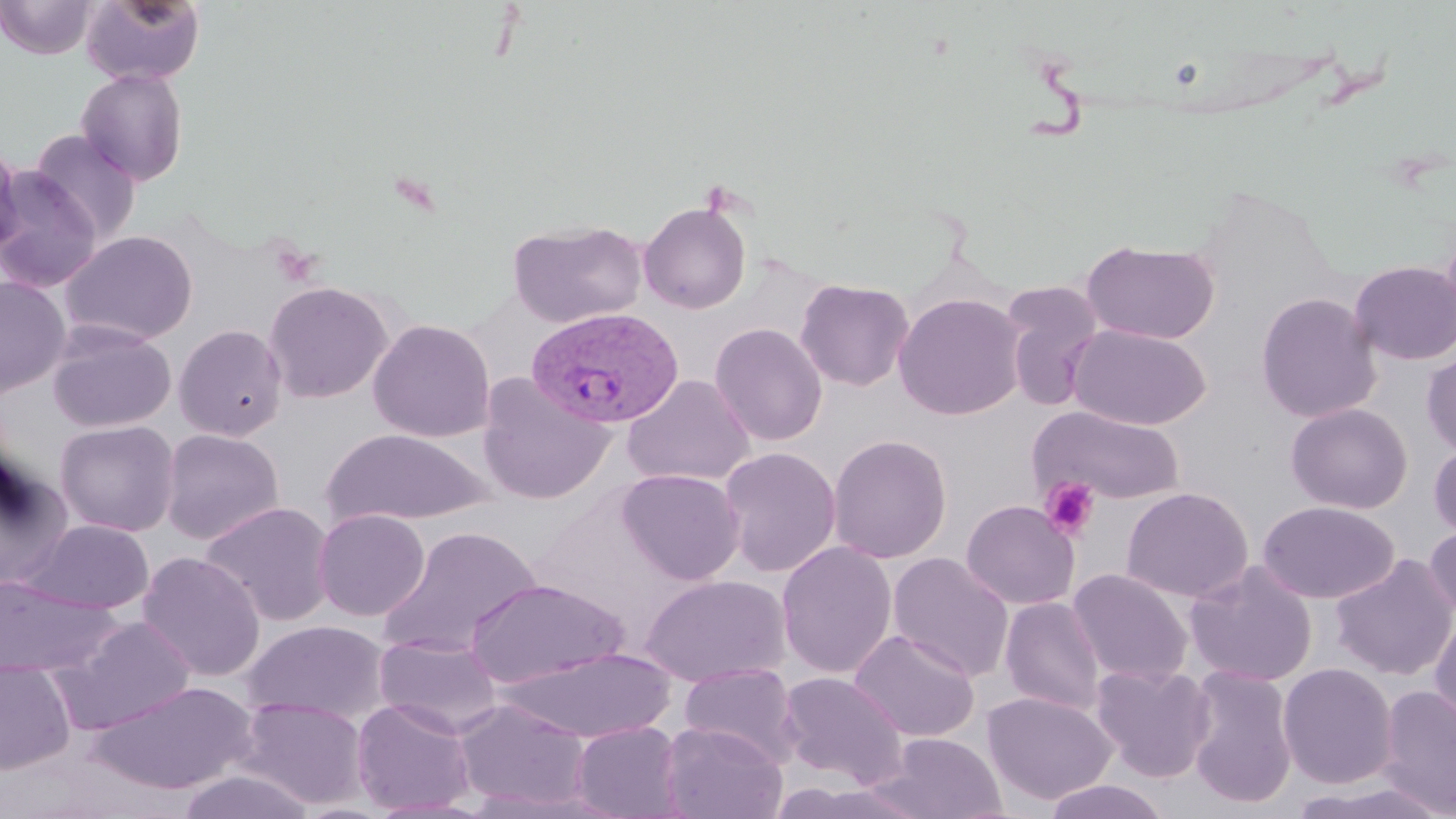
Summary:
  - Coordinate format: approximate bounding boxes as (x1, y1, x2, y2) in pixels
  - Plasmodium vivax-infected red blood cell locations: (527, 307, 683, 430)
  - Uninfected red blood cell locations: (1, 0, 95, 59), (81, 0, 206, 85), (76, 68, 189, 186), (30, 129, 142, 243), (0, 146, 24, 256), (0, 167, 103, 290), (638, 198, 752, 314), (507, 220, 647, 328), (61, 231, 198, 345), (1081, 238, 1219, 345), (1349, 260, 1456, 365), (0, 276, 70, 399), (795, 278, 914, 391), (263, 280, 393, 404), (1001, 281, 1105, 411), (893, 292, 1027, 420), (1256, 292, 1382, 422), (368, 318, 496, 443), (48, 323, 176, 433), (710, 323, 828, 446), (173, 324, 288, 441), (1067, 324, 1212, 430), (1421, 348, 1456, 457), (477, 375, 615, 505), (622, 375, 756, 487), (1285, 402, 1412, 514), (1029, 405, 1187, 505), (54, 420, 180, 537), (160, 429, 283, 544), (320, 429, 496, 527), (828, 434, 952, 564), (1428, 440, 1456, 544), (719, 447, 841, 578), (0, 463, 74, 589), (617, 468, 745, 585), (1121, 487, 1252, 602), (961, 499, 1080, 610), (1257, 500, 1400, 604), (200, 502, 336, 627), (313, 509, 430, 621), (21, 519, 155, 614), (1424, 522, 1456, 621), (376, 526, 543, 659), (776, 541, 898, 680), (137, 551, 266, 681), (887, 552, 1014, 682), (1328, 554, 1455, 681), (1184, 561, 1317, 687), (1067, 568, 1193, 686), (0, 575, 119, 677), (640, 575, 791, 687), (466, 578, 629, 689), (1000, 597, 1107, 716), (1429, 610, 1456, 732), (54, 616, 196, 734), (242, 619, 391, 725), (849, 629, 980, 741), (373, 633, 504, 737), (501, 647, 677, 743), (0, 659, 76, 774), (679, 662, 802, 767), (1091, 662, 1216, 782), (1278, 662, 1398, 790), (1184, 666, 1298, 810), (778, 671, 909, 787), (88, 680, 258, 794), (1376, 685, 1456, 817), (983, 691, 1117, 805), (234, 695, 370, 809), (351, 698, 476, 815), (452, 698, 593, 812), (570, 721, 686, 818), (658, 721, 786, 819), (878, 733, 1006, 819), (175, 769, 317, 819), (1287, 779, 1454, 819), (1040, 780, 1174, 819)
  - Platelet locations: (1040, 477, 1101, 541)
  - Slide-level diagnosis: Plasmodium vivax
  - Image size: 1456×819 pixels
  - Modality: light microscopy
  - Preparation: thin blood film
  - Magnification: 1000x
  - Stain: May-Grünwald-Giemsa
  - Field of view: one of a larger specimen